Assess the morphology of the erythrocytes.
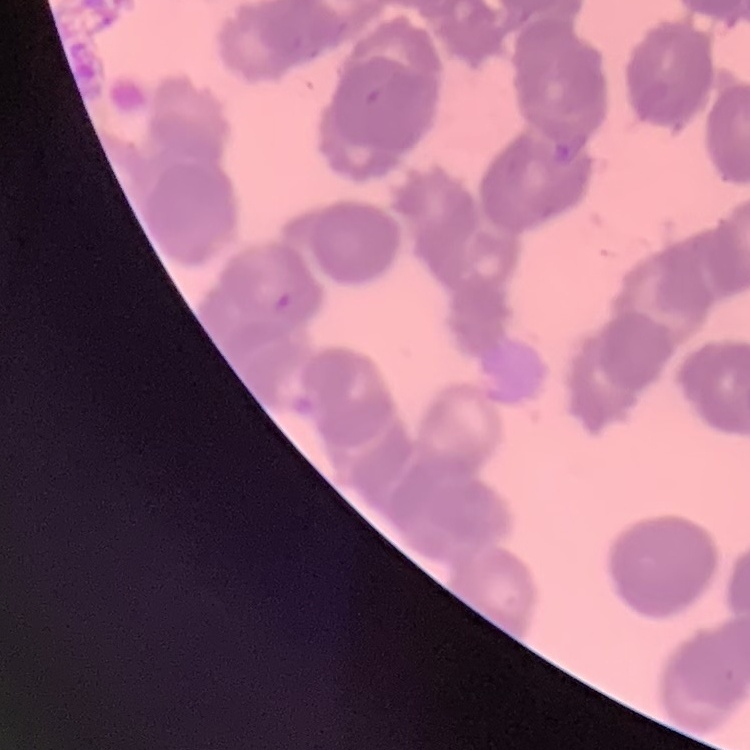
They show rouleaux formation.

One tile cut from a larger photomicrograph. Thin peripheral smear. Field's or Giemsa stain.